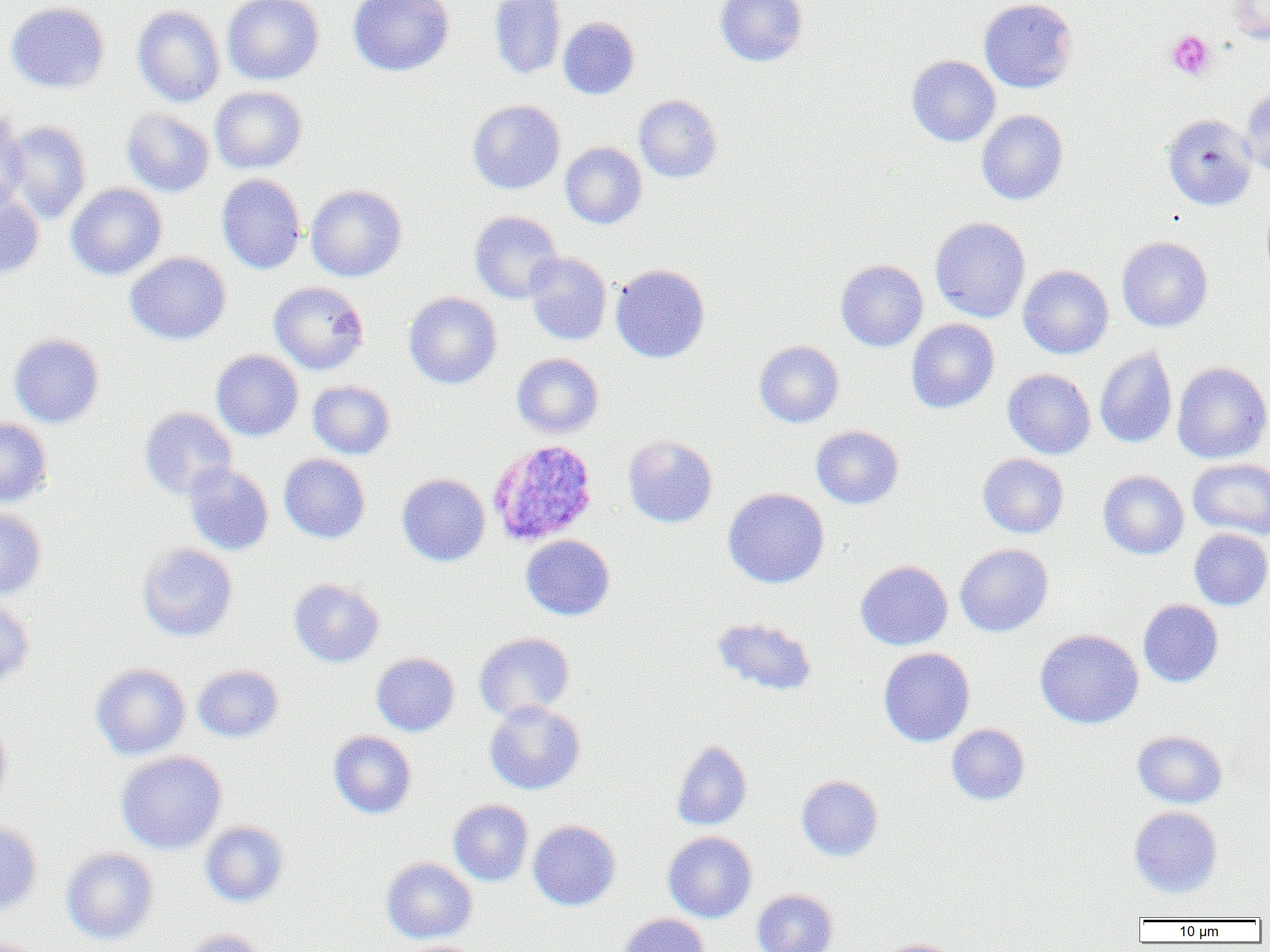

{
  "plasmodium_ovale_infected_red_blood_cell_locations": "approximate bounding boxes as [x1, y1, x2, y2] in pixels: [488, 439, 598, 546]",
  "slide_level_diagnosis": "Plasmodium ovale",
  "preparation": "thin blood smear",
  "platelet_locations": "approximate bounding boxes as [x1, y1, x2, y2] in pixels: [1165, 30, 1217, 81]",
  "magnification": "1000x",
  "field_of_view": "single",
  "image_size": "1270×952 pixels",
  "modality": "light microscopy",
  "uninfected_red_blood_cell_locations": "approximate bounding boxes as [x1, y1, x2, y2] in pixels: [222, 0, 324, 85], [347, 0, 454, 76], [488, 0, 567, 79], [715, 0, 807, 67], [978, 0, 1077, 93], [6, 1, 109, 93], [1226, 1, 1270, 44], [132, 5, 226, 107], [558, 17, 639, 99], [907, 55, 1000, 146], [209, 86, 307, 174], [1240, 86, 1270, 178], [634, 95, 722, 183], [468, 99, 565, 194], [121, 108, 214, 197], [0, 110, 29, 209], [977, 110, 1068, 205], [1162, 113, 1257, 211], [2, 120, 92, 224], [560, 142, 647, 229], [216, 174, 306, 274], [66, 183, 167, 279], [306, 184, 407, 282], [0, 187, 44, 278], [469, 211, 564, 304], [929, 217, 1031, 323], [1116, 236, 1213, 332], [124, 252, 231, 344], [523, 253, 612, 345], [836, 259, 928, 351], [611, 263, 710, 363], [1018, 265, 1113, 359], [268, 281, 369, 375], [404, 292, 502, 389], [906, 319, 999, 413], [9, 333, 105, 428], [754, 340, 844, 427], [1095, 347, 1177, 447], [211, 350, 303, 441], [512, 353, 604, 438], [1172, 362, 1270, 464], [1002, 368, 1095, 459], [307, 381, 395, 459], [139, 407, 237, 500], [0, 418, 53, 507], [811, 425, 903, 509], [623, 434, 717, 528], [279, 453, 370, 543], [978, 453, 1069, 538], [1187, 458, 1270, 539], [184, 462, 273, 556], [1098, 470, 1189, 559], [397, 473, 490, 566], [723, 488, 829, 588], [0, 507, 47, 601], [1188, 528, 1270, 610], [520, 534, 614, 620], [137, 543, 238, 642], [955, 543, 1054, 637], [855, 560, 952, 650], [288, 578, 384, 668], [1138, 599, 1223, 687], [0, 600, 35, 689], [711, 618, 817, 696], [1035, 629, 1143, 729], [473, 632, 574, 721], [878, 647, 975, 746], [371, 652, 459, 736], [90, 663, 191, 760], [193, 665, 283, 742], [484, 701, 585, 795], [0, 716, 12, 813], [947, 723, 1029, 805], [328, 730, 416, 818], [1132, 730, 1227, 809], [671, 739, 753, 831], [115, 750, 227, 854], [796, 775, 883, 860], [448, 799, 533, 886], [1129, 806, 1222, 897], [0, 820, 42, 916], [200, 820, 290, 907], [528, 820, 620, 911], [662, 831, 757, 923], [61, 847, 160, 945], [381, 857, 477, 943], [752, 889, 838, 952], [618, 913, 710, 952], [180, 929, 265, 952], [876, 938, 964, 952]"
}